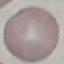

result = negative for malaria parasites
capture = smartphone camera at the microscope eyepiece
stain = Giemsa
preparation = thin blood smear
image type = cell patch, automatically extracted from a larger field of view and resized to 64 × 64 pixels